Locate every uninfected red blood cell.
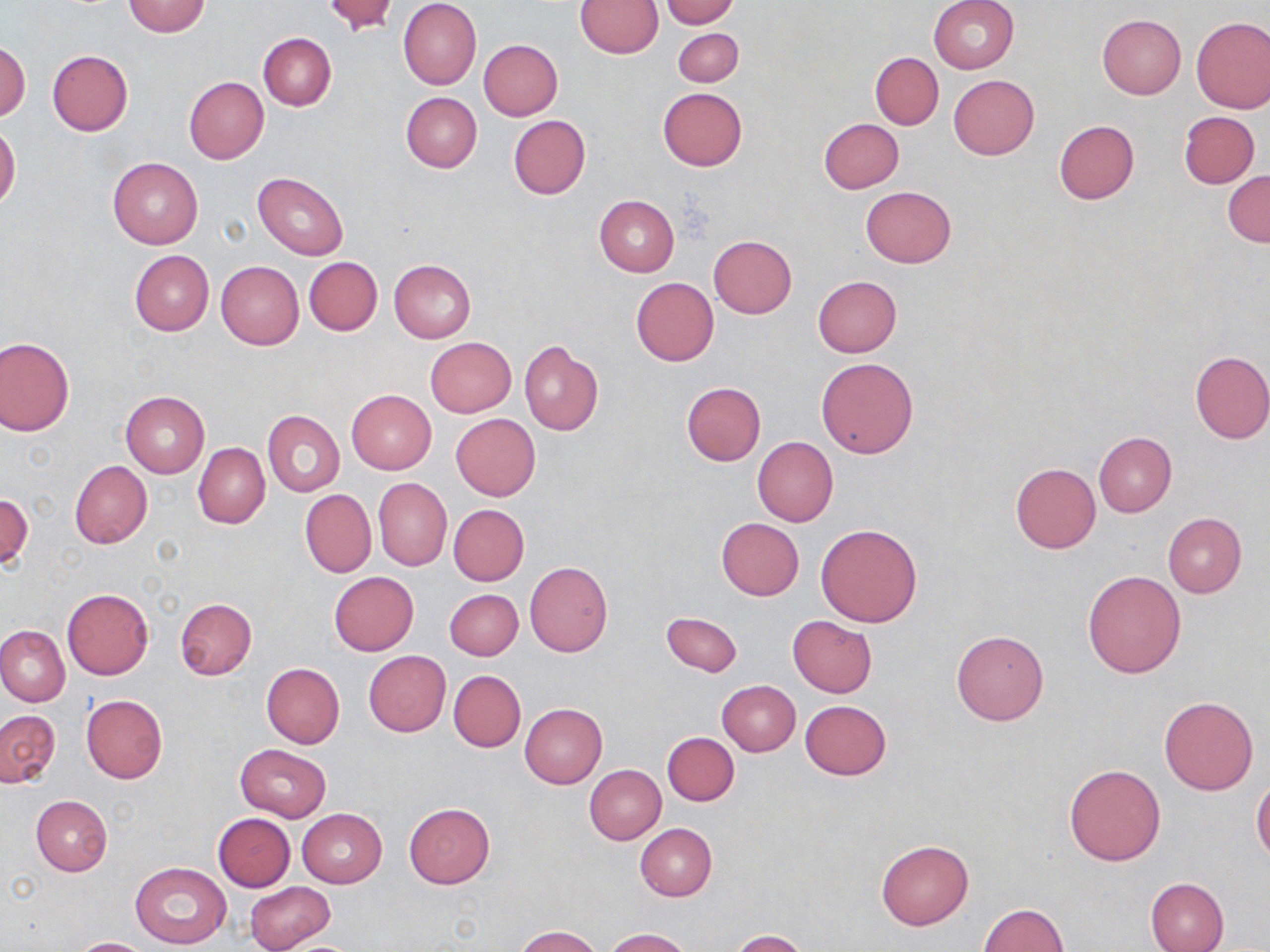
Approximate bounding boxes as (x1, y1, x2, y2) in pixels.
Uninfected red blood cells: (322, 0, 399, 33), (662, 0, 740, 28), (928, 0, 1018, 74), (122, 1, 211, 37), (399, 1, 481, 90), (574, 2, 663, 57), (1097, 15, 1186, 98), (1192, 17, 1270, 113), (672, 28, 744, 86), (258, 33, 336, 111), (479, 39, 563, 120), (0, 41, 30, 122), (47, 50, 133, 135), (870, 53, 943, 129), (949, 74, 1039, 159), (184, 77, 268, 164), (657, 88, 746, 171), (401, 92, 481, 173), (1178, 110, 1259, 189), (508, 115, 590, 199), (819, 118, 903, 192), (1053, 120, 1139, 203), (0, 122, 20, 212), (108, 156, 203, 248), (1224, 171, 1270, 247), (252, 172, 349, 260), (861, 186, 956, 267), (594, 195, 679, 276), (708, 235, 797, 318), (129, 250, 213, 336), (305, 257, 382, 336), (389, 258, 476, 342), (216, 261, 303, 349), (812, 275, 902, 357), (630, 277, 718, 366), (1, 336, 75, 434), (425, 337, 517, 417), (518, 340, 603, 436), (1189, 350, 1270, 444), (816, 358, 918, 458), (681, 382, 766, 465), (346, 390, 436, 474), (121, 391, 209, 477), (263, 410, 345, 497), (451, 414, 540, 500), (1093, 431, 1176, 516), (753, 437, 838, 526), (192, 441, 270, 529), (69, 461, 153, 549), (1010, 463, 1100, 554), (374, 479, 451, 570), (300, 489, 376, 578), (1, 492, 33, 571), (448, 504, 529, 585), (1163, 513, 1246, 597), (716, 518, 804, 600), (817, 524, 921, 627), (525, 560, 614, 657), (1083, 570, 1186, 677), (329, 572, 419, 655), (445, 588, 523, 660), (62, 589, 153, 679), (175, 598, 257, 680), (661, 611, 741, 676), (788, 616, 876, 698), (0, 624, 70, 707), (951, 629, 1049, 726), (363, 651, 452, 737), (261, 662, 345, 748), (448, 670, 526, 752), (717, 681, 800, 756), (80, 695, 167, 784), (1159, 696, 1258, 794), (799, 700, 891, 780), (519, 703, 606, 790), (0, 710, 60, 787), (662, 732, 739, 806), (235, 744, 330, 822), (1064, 764, 1166, 866), (584, 765, 666, 844), (1251, 779, 1270, 863), (30, 795, 113, 875), (404, 803, 495, 888), (296, 808, 388, 888), (213, 813, 296, 891), (635, 822, 717, 901), (876, 840, 973, 929), (130, 861, 232, 948), (1145, 877, 1228, 952), (246, 883, 332, 950), (978, 903, 1068, 952), (515, 926, 603, 952), (601, 928, 692, 951), (729, 929, 808, 952), (67, 937, 155, 952), (273, 939, 366, 952).

slide-level diagnosis = no evidence of blood parasites
modality = optical microscopy
preparation = thin blood film
field of view = one of a larger specimen
magnification = 1000x
stain = May-Grünwald-Giemsa
image size = 1270×952 pixels